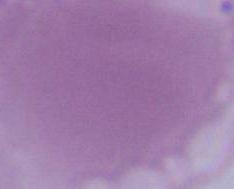 Micrograph. Captured at 1000x magnification. A red blood cell is seen.